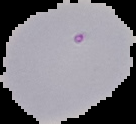
result = Plasmodium parasites identified
image size = 136×124 pixels
image type = segmented cell region with the area outside set to black
preparation = thin blood film